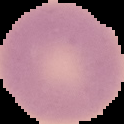
malaria status = uninfected
image type = segmented cell region on a black background
image size = 124×124 pixels
preparation = thin blood smear